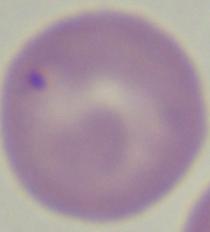

A Babesia parasite is seen. Micrograph. 1000x magnification.